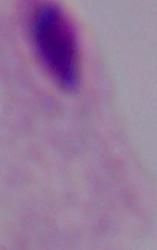
identification = trichomonad
modality = micrograph
magnification = 1000x